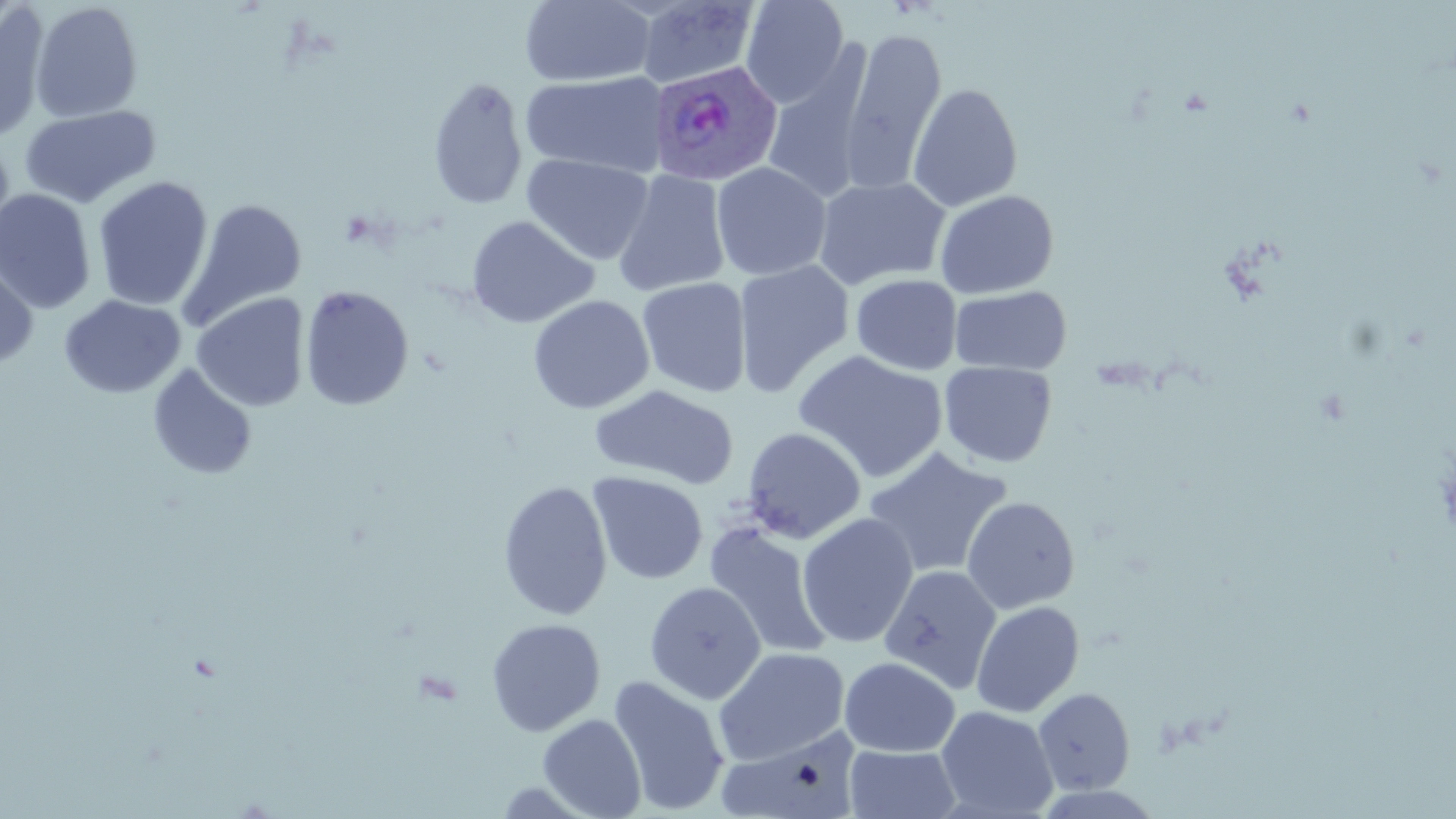
Summary:
  - Coordinate format: approximate bounding boxes as (x1,y1)-(x2,y2) corner pairs in pixels
  - Plasmodium ovale-infected red blood cell locations: (650,60)-(783,187)
  - Uninfected red blood cell locations: (740,0)-(849,108), (520,1)-(655,87), (634,1)-(761,89), (0,2)-(51,144), (31,2)-(143,123), (838,27)-(947,196), (763,47)-(873,206), (521,71)-(667,178), (428,75)-(528,210), (423,76)-(637,201), (907,83)-(1022,212), (19,105)-(160,208), (0,137)-(17,257), (521,153)-(654,265), (711,162)-(832,281), (612,170)-(731,297), (92,176)-(213,311), (812,176)-(951,291), (0,189)-(97,314), (934,189)-(1059,298), (179,199)-(307,332), (466,216)-(599,329), (0,255)-(38,370), (733,260)-(855,397), (851,274)-(962,375), (637,278)-(752,398), (299,285)-(414,411), (949,285)-(1072,375), (191,293)-(310,412), (59,295)-(186,399), (528,295)-(655,414), (793,350)-(948,483), (939,361)-(1057,467), (147,364)-(257,480), (589,384)-(739,489), (742,426)-(867,544), (863,446)-(1013,579), (588,471)-(708,585), (497,480)-(613,620), (961,496)-(1080,614), (797,513)-(919,648), (702,520)-(833,660), (878,563)-(1002,695), (644,581)-(766,704), (970,600)-(1084,718), (485,618)-(605,736), (713,647)-(850,764), (839,656)-(960,757), (608,674)-(730,815), (1033,687)-(1135,794), (936,706)-(1059,818), (537,713)-(646,818), (715,730)-(859,818), (844,744)-(961,819)
  - Slide-level diagnosis: Plasmodium ovale
  - Magnification: 1000x
  - Preparation: thin blood film
  - Stain: May-Grünwald-Giemsa
  - Field of view: one of a larger specimen
  - Modality: light microscopy
  - Image size: 1456×819 pixels